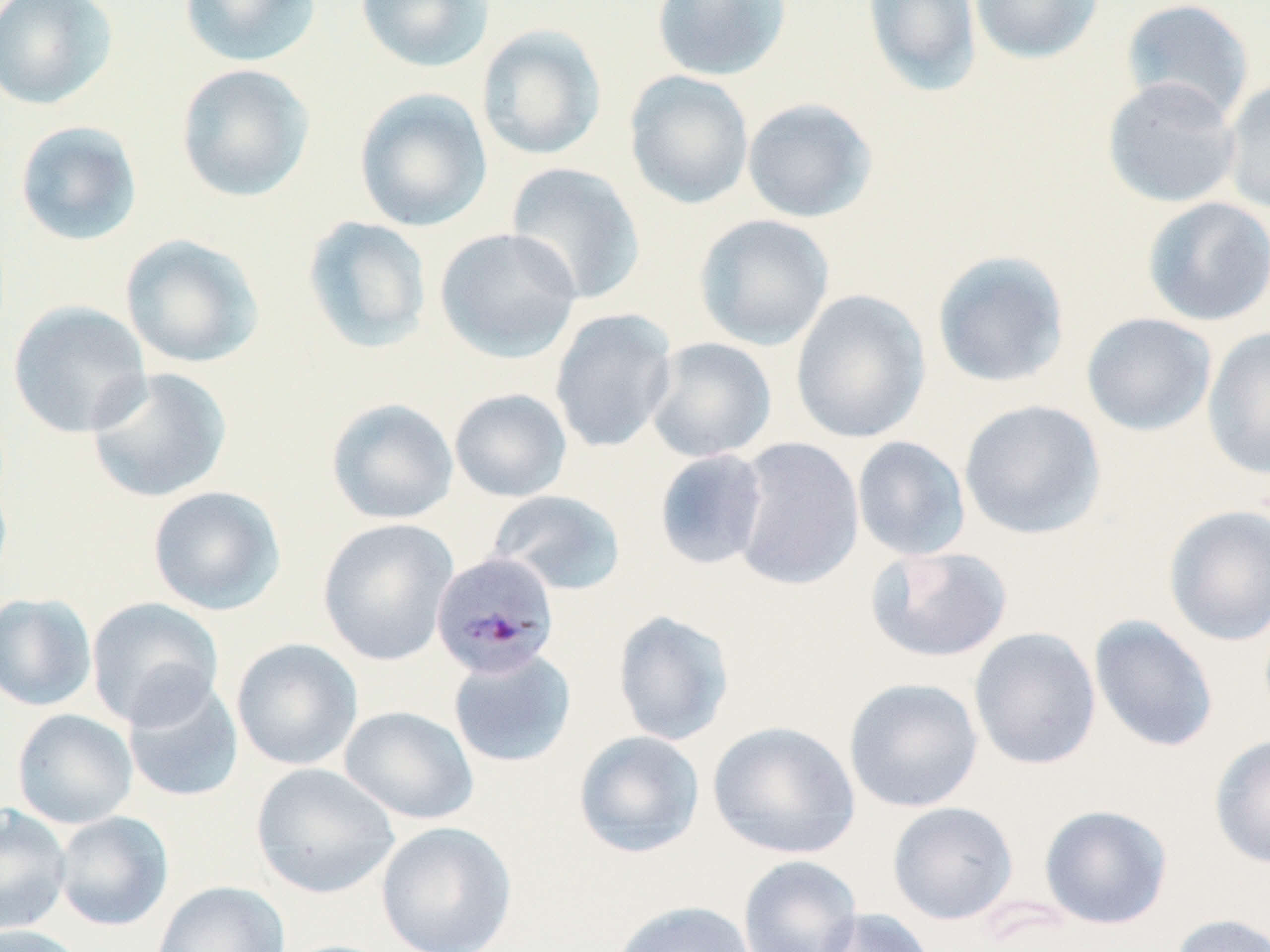

Approximate bounding boxes as (x1, y1, x2, y2) in pixels. Uninfected red blood cell locations: (0, 0, 119, 110), (178, 0, 322, 69), (355, 0, 495, 74), (650, 0, 792, 82), (862, 0, 982, 97), (970, 0, 1104, 64), (1119, 0, 1255, 124), (476, 24, 608, 162), (175, 63, 316, 203), (624, 71, 754, 210), (1102, 76, 1242, 208), (1221, 76, 1270, 217), (353, 87, 493, 233), (741, 97, 878, 223), (13, 120, 144, 247), (504, 162, 646, 305), (1141, 196, 1270, 327), (694, 214, 835, 351), (302, 215, 433, 354), (434, 227, 582, 363), (119, 234, 266, 369), (931, 250, 1071, 389), (789, 289, 931, 445), (7, 300, 153, 439), (549, 308, 678, 454), (1081, 312, 1217, 436), (1201, 326, 1270, 479), (643, 336, 777, 463), (84, 366, 233, 504), (449, 388, 572, 503), (325, 397, 459, 525), (958, 399, 1106, 541), (851, 436, 971, 561), (729, 437, 865, 591), (653, 449, 769, 571), (147, 485, 286, 615), (487, 489, 627, 596), (1163, 504, 1270, 646), (317, 518, 459, 666), (865, 545, 1014, 663), (0, 592, 97, 712), (86, 596, 224, 729), (612, 609, 735, 746), (1089, 615, 1219, 753), (969, 626, 1102, 770), (231, 638, 363, 770), (447, 647, 577, 768), (122, 675, 244, 803), (843, 677, 983, 813), (339, 705, 479, 825), (12, 709, 138, 829), (707, 720, 861, 860), (573, 730, 705, 858), (1209, 734, 1270, 869), (251, 762, 400, 898), (887, 801, 1019, 925), (0, 804, 72, 935), (1039, 804, 1173, 929), (53, 811, 173, 932), (376, 821, 517, 952), (737, 855, 863, 952), (152, 880, 291, 951), (610, 900, 757, 952), (815, 907, 935, 952), (1167, 912, 1270, 952), (0, 924, 88, 952). Plasmodium malariae-infected red blood cell locations: (431, 552, 560, 679). Slide-level diagnosis: Plasmodium malariae. Single field of view. Image is 1270×952 pixels. 1000x magnification. May-Grünwald-Giemsa stain. Thin blood film. Optical microscopy.